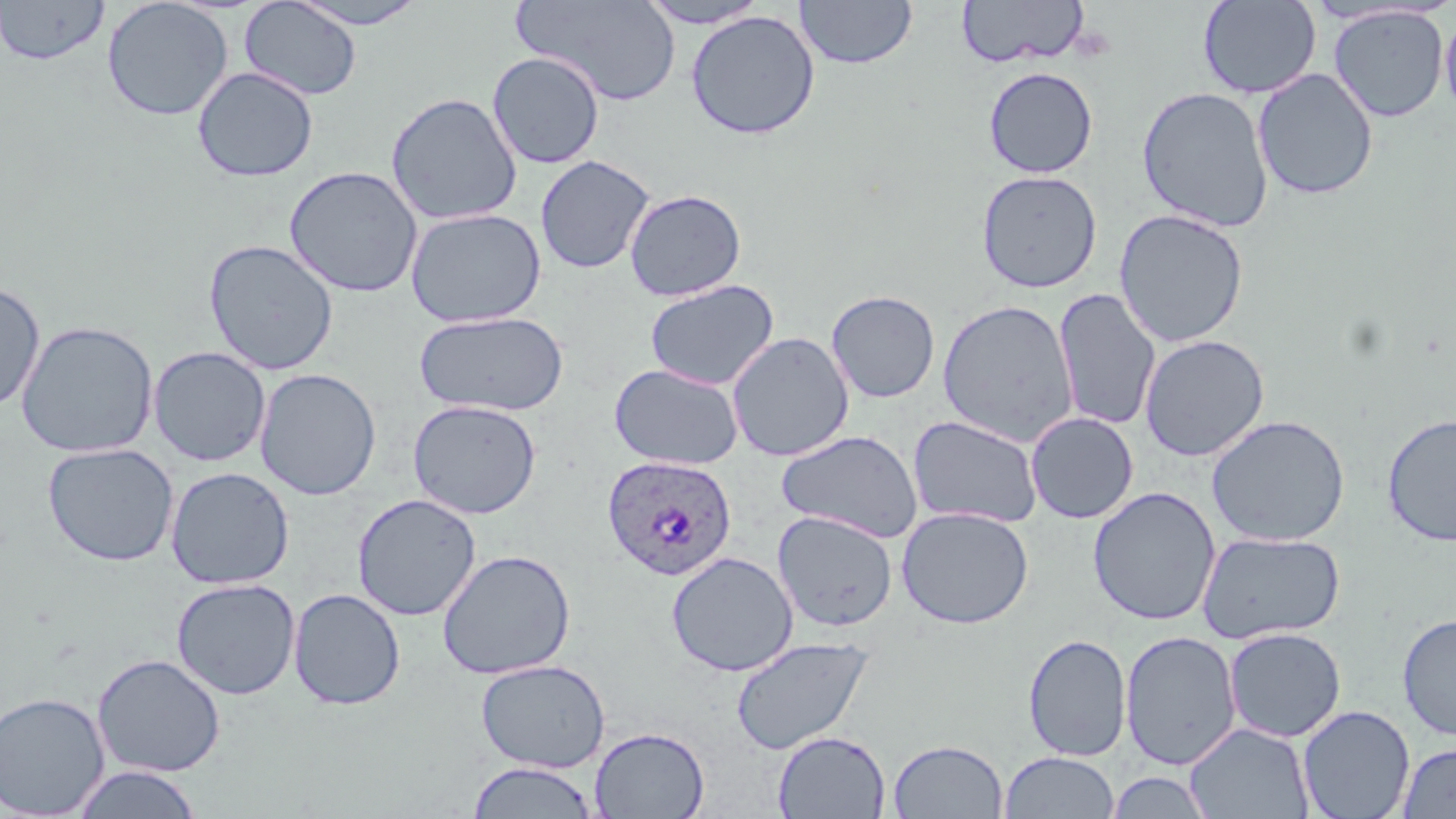
slide-level diagnosis = Plasmodium ovale
stain = May-Grünwald-Giemsa
Plasmodium ovale-infected red blood cell locations = approximate bounding boxes as [x1, y1, x2, y2] in pixels: [602, 455, 737, 581]
image size = 1456×819 pixels
preparation = thin blood film
modality = optical microscopy
uninfected red blood cell locations = approximate bounding boxes as [x1, y1, x2, y2] in pixels: [0, 0, 110, 66], [102, 0, 233, 121], [287, 0, 431, 29], [513, 0, 683, 105], [638, 0, 771, 29], [794, 0, 917, 70], [1198, 0, 1321, 99], [239, 1, 362, 100], [956, 1, 1089, 68], [1328, 5, 1449, 123], [685, 10, 820, 140], [1440, 11, 1456, 120], [487, 52, 605, 169], [192, 67, 319, 182], [983, 67, 1098, 178], [1252, 68, 1378, 200], [1136, 86, 1274, 233], [385, 92, 523, 225], [535, 155, 655, 274], [283, 165, 423, 298], [976, 170, 1103, 293], [624, 189, 747, 301], [405, 208, 547, 327], [1113, 209, 1249, 347], [203, 239, 339, 376], [644, 279, 780, 391], [0, 281, 45, 414], [1053, 288, 1161, 432], [826, 290, 941, 403], [937, 299, 1079, 446], [414, 310, 568, 416], [16, 320, 158, 458], [726, 331, 855, 461], [1139, 334, 1270, 461], [148, 346, 271, 467], [609, 363, 743, 470], [254, 368, 382, 500], [407, 399, 542, 519], [1026, 412, 1138, 524], [1381, 412, 1456, 545], [1206, 413, 1350, 547], [908, 416, 1043, 528], [775, 430, 923, 542], [42, 442, 179, 566], [165, 467, 294, 590], [1088, 486, 1221, 626], [352, 493, 481, 621], [896, 506, 1034, 629], [773, 511, 898, 632], [1197, 531, 1345, 644], [437, 549, 576, 679], [666, 551, 798, 676], [171, 578, 301, 700], [289, 588, 406, 710], [1397, 613, 1456, 741], [1223, 627, 1346, 742], [1120, 630, 1241, 770], [1022, 633, 1132, 761], [731, 636, 874, 755], [92, 653, 226, 777], [475, 659, 610, 773], [0, 692, 110, 817], [1297, 705, 1415, 819], [1184, 722, 1314, 818], [589, 726, 710, 819], [773, 730, 890, 818], [888, 739, 1008, 818], [1396, 743, 1456, 818], [999, 751, 1119, 818], [467, 761, 600, 818], [70, 765, 203, 818], [1105, 771, 1214, 818]
field of view = single
magnification = 1000x